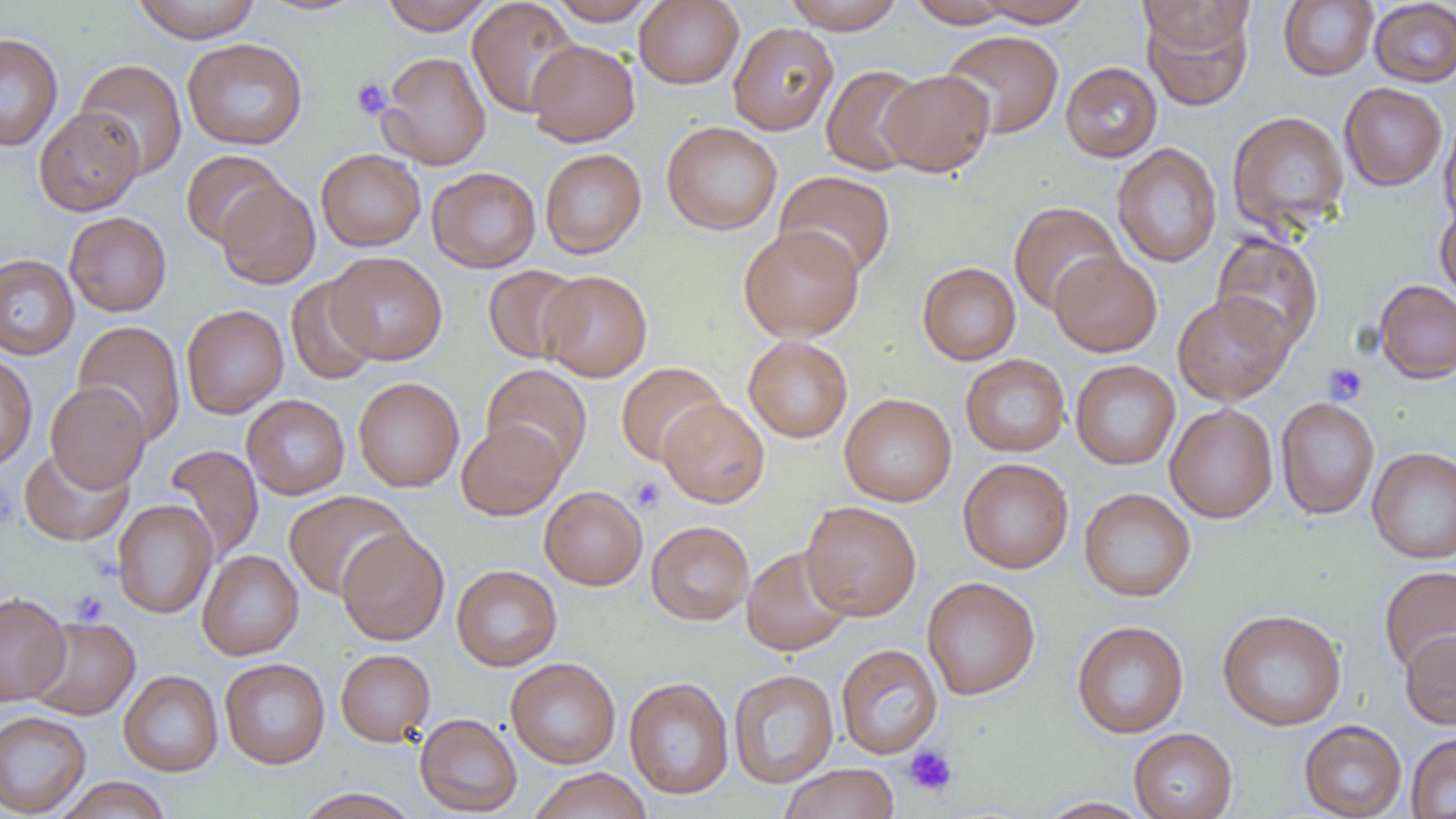

Summary:
  - Coordinate format: approximate bounding boxes as (x1, y1, x2, y2) in pixels
  - Platelet locations: (351, 77, 393, 120), (1323, 362, 1367, 405), (629, 477, 666, 513), (70, 590, 109, 627), (903, 744, 959, 797)
  - Uninfected red blood cell locations: (131, 0, 262, 43), (257, 0, 370, 16), (379, 0, 495, 35), (467, 0, 581, 117), (546, 0, 660, 25), (634, 0, 744, 89), (783, 0, 905, 33), (975, 0, 1094, 27), (1136, 0, 1254, 55), (1278, 0, 1378, 80), (1368, 0, 1456, 87), (907, 1, 1018, 28), (1142, 6, 1254, 110), (727, 22, 838, 135), (940, 30, 1064, 140), (0, 32, 63, 151), (182, 37, 308, 151), (526, 39, 640, 146), (378, 51, 491, 169), (75, 58, 187, 179), (1061, 61, 1162, 162), (821, 65, 927, 176), (879, 69, 994, 177), (1339, 83, 1448, 191), (33, 107, 144, 216), (1226, 110, 1350, 235), (1439, 112, 1456, 231), (662, 121, 782, 235), (1112, 142, 1222, 268), (316, 148, 426, 251), (540, 148, 646, 258), (181, 150, 286, 248), (427, 166, 541, 273), (775, 170, 896, 279), (216, 179, 320, 289), (1008, 201, 1125, 314), (1435, 203, 1456, 306), (64, 212, 172, 317), (739, 225, 864, 342), (1211, 231, 1323, 352), (327, 251, 447, 365), (1049, 251, 1162, 357), (0, 254, 80, 360), (917, 261, 1021, 365), (482, 264, 585, 364), (539, 270, 652, 382), (286, 276, 382, 385), (1373, 280, 1456, 384), (1173, 293, 1294, 405), (181, 304, 288, 419), (73, 320, 186, 446), (743, 335, 853, 442), (0, 353, 37, 471), (960, 354, 1070, 457), (1070, 359, 1180, 470), (615, 362, 727, 466), (482, 364, 593, 475), (353, 377, 464, 492), (46, 382, 150, 493), (839, 393, 957, 506), (241, 394, 350, 499), (1276, 397, 1379, 519), (658, 398, 770, 507), (1165, 403, 1278, 523), (456, 419, 566, 520), (164, 443, 263, 563), (19, 446, 134, 546), (1367, 446, 1456, 563), (958, 458, 1074, 573), (539, 486, 647, 590), (1079, 488, 1196, 602), (284, 491, 412, 600), (112, 499, 218, 619), (801, 501, 921, 621), (646, 520, 754, 625), (336, 527, 449, 645), (742, 546, 853, 656), (197, 550, 304, 660), (451, 565, 562, 671), (1379, 565, 1456, 677), (922, 576, 1040, 700), (0, 592, 71, 706), (1217, 608, 1347, 731), (27, 615, 140, 720), (1072, 620, 1189, 738), (1400, 629, 1456, 729), (836, 643, 943, 759), (336, 648, 435, 745), (219, 657, 330, 769), (506, 657, 621, 769), (728, 669, 839, 788), (119, 670, 223, 776), (623, 676, 734, 800), (0, 711, 91, 817), (414, 713, 522, 816), (1299, 719, 1407, 819), (1128, 728, 1238, 818), (1406, 733, 1456, 819), (778, 763, 900, 819), (528, 767, 651, 819), (54, 776, 172, 819), (294, 787, 422, 819), (1036, 797, 1153, 818)
  - Slide-level diagnosis: no evidence of blood parasites
  - Preparation: thin blood smear
  - Image size: 1456×819 pixels
  - Field of view: one of a larger specimen
  - Magnification: 1000x
  - Modality: optical microscopy